Describe the morphology of the red blood cells.
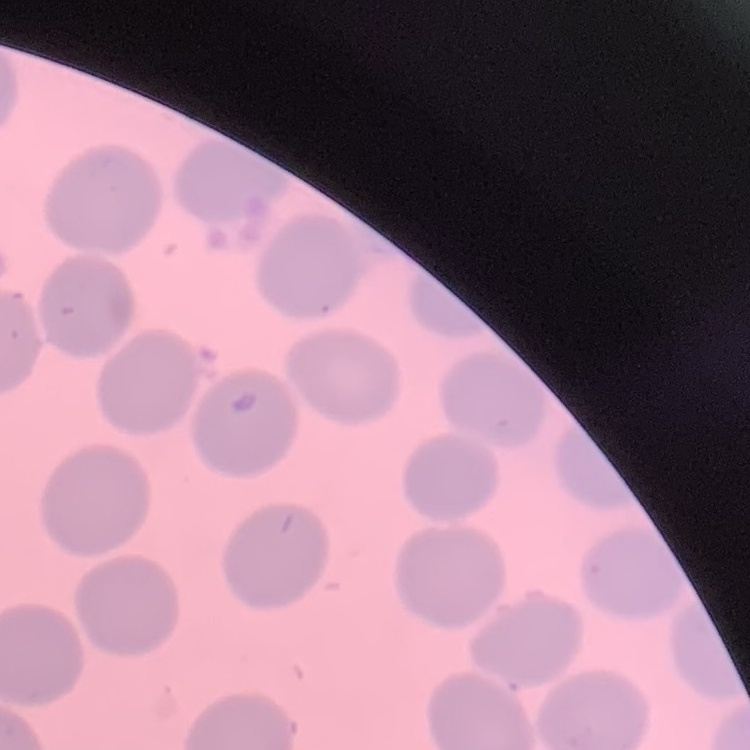

No rouleaux formation.

{
  "image_type": "square crop of a larger photomicrograph",
  "preparation": "thin blood film",
  "stain": "Field's or Giemsa"
}